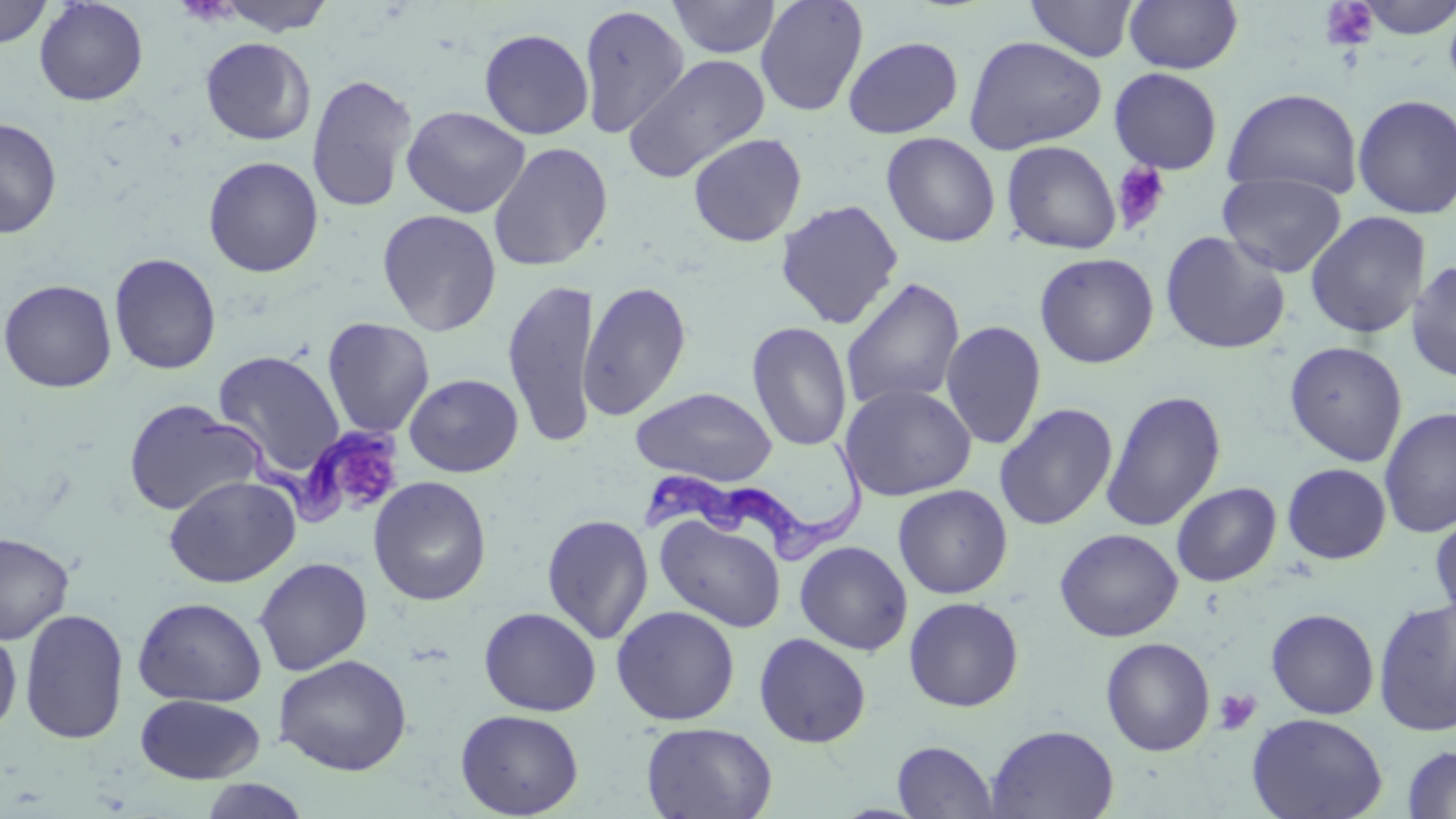
Summary:
  - Coordinate format: approximate bounding boxes as (x1, y1, x2, y2) in pixels
  - Trypanosoma brucei locations: (200, 415, 397, 527), (639, 442, 880, 566)
  - Uninfected red blood cell locations: (0, 0, 53, 50), (33, 0, 148, 105), (213, 0, 336, 36), (667, 0, 781, 59), (754, 0, 869, 116), (1123, 0, 1243, 73), (1352, 0, 1456, 40), (1025, 1, 1139, 62), (1443, 2, 1456, 102), (577, 4, 690, 140), (478, 27, 594, 139), (963, 35, 1107, 154), (200, 36, 316, 146), (843, 36, 964, 138), (624, 52, 771, 183), (1109, 67, 1224, 174), (306, 72, 417, 213), (1223, 87, 1363, 200), (1352, 93, 1456, 219), (401, 105, 531, 218), (0, 116, 62, 238), (687, 132, 807, 247), (881, 132, 1001, 247), (1001, 140, 1122, 254), (488, 141, 613, 271), (203, 155, 324, 278), (1218, 172, 1347, 277), (775, 198, 904, 329), (376, 208, 503, 336), (1304, 210, 1432, 339), (1159, 230, 1291, 355), (108, 252, 222, 375), (1035, 252, 1159, 368), (1405, 259, 1456, 381), (840, 276, 966, 412), (502, 277, 599, 448), (0, 278, 117, 393), (578, 280, 693, 421), (322, 317, 435, 438), (747, 320, 853, 453), (940, 320, 1047, 450), (1284, 340, 1408, 467), (212, 350, 346, 479), (404, 373, 523, 477), (839, 382, 977, 501), (630, 386, 779, 486), (1101, 389, 1227, 532), (122, 398, 262, 517), (994, 403, 1118, 530), (1379, 405, 1456, 538), (1282, 462, 1392, 564), (164, 475, 301, 588), (368, 476, 492, 606), (1171, 481, 1281, 586), (893, 484, 1013, 599), (1430, 510, 1456, 623), (541, 513, 654, 644), (655, 514, 787, 633), (1055, 528, 1183, 641), (0, 532, 74, 644), (794, 540, 913, 655), (253, 556, 373, 676), (132, 596, 267, 707), (903, 596, 1024, 712), (1373, 597, 1456, 737), (611, 605, 741, 725), (479, 606, 602, 716), (19, 607, 130, 744), (1265, 608, 1380, 719), (0, 628, 22, 736), (753, 632, 871, 747), (1100, 637, 1216, 756), (273, 653, 412, 775), (135, 693, 265, 784), (455, 708, 585, 818), (1246, 712, 1388, 819), (641, 722, 777, 818), (986, 724, 1119, 819), (892, 740, 999, 818), (1402, 745, 1456, 818), (197, 778, 311, 819)
  - Platelet locations: (1319, 1, 1380, 52), (1111, 162, 1171, 233), (345, 456, 391, 499), (1212, 688, 1262, 735)
  - Slide-level diagnosis: Trypanosoma brucei
  - Image size: 1456×819 pixels
  - Modality: light microscopy
  - Preparation: thin blood smear
  - Field of view: single
  - Magnification: 1000x
  - Stain: May-Grünwald-Giemsa